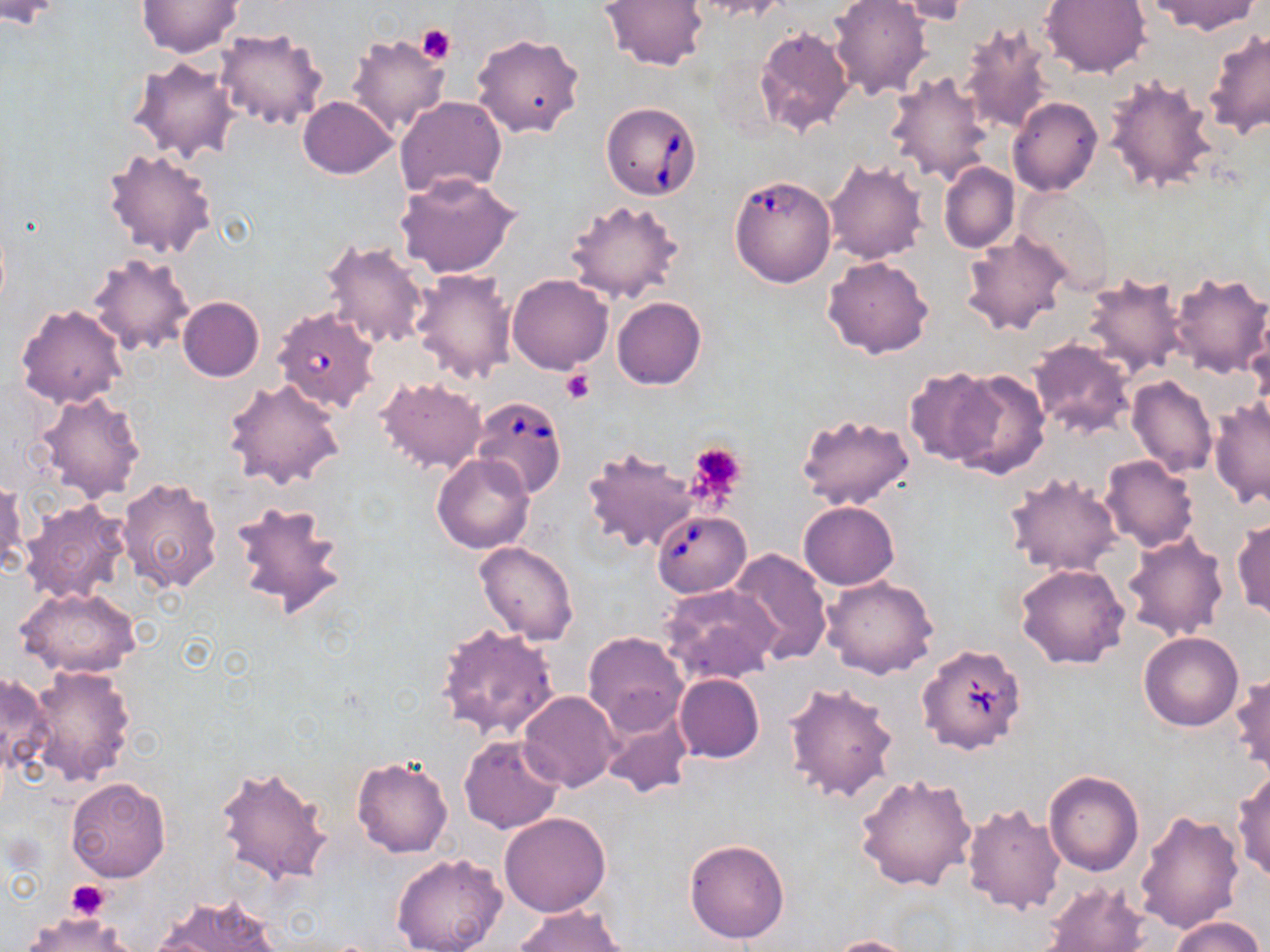
slide_level_diagnosis: Babesia divergens
preparation: thin blood smear
field_of_view: one of a larger specimen
platelet_locations: 'approximate bounding boxes as (x1,y1)-(x2,y2) corner pairs in pixels: (416,24)-(456,65), (560,370)-(594,405), (686,441)-(747,502), (66,880)-(109,920)'
magnification: 1000x
uninfected_red_blood_cell_locations: 'approximate bounding boxes as (x1,y1)-(x2,y2) corner pairs in pixels: (136,0)-(243,57), (601,0)-(709,70), (692,0)-(788,20), (828,0)-(933,102), (1041,0)-(1152,78), (1146,0)-(1260,35), (0,1)-(67,29), (887,1)-(972,26), (957,21)-(1056,136), (215,26)-(328,131), (753,26)-(855,137), (1203,30)-(1270,139), (345,33)-(450,136), (472,33)-(586,139), (127,55)-(239,162), (886,71)-(995,186), (1104,75)-(1221,195), (297,96)-(397,179), (394,96)-(507,199), (1008,98)-(1102,196), (101,146)-(219,259), (824,158)-(929,265), (939,162)-(1019,254), (395,172)-(521,278), (1015,187)-(1116,295), (565,198)-(686,305), (961,232)-(1070,338), (321,239)-(429,350), (88,252)-(196,357), (822,256)-(935,358), (410,267)-(518,385), (1081,270)-(1189,381), (1167,270)-(1270,379), (507,274)-(613,374), (177,297)-(265,382), (613,297)-(707,390), (15,303)-(128,409), (271,306)-(382,414), (1248,333)-(1270,434), (1027,339)-(1136,441), (903,366)-(1001,465), (945,368)-(1050,477), (1127,375)-(1218,478), (376,376)-(487,473), (223,377)-(347,492), (34,391)-(146,503), (1208,398)-(1269,509), (796,413)-(915,511), (582,446)-(697,555), (432,453)-(535,553), (1100,455)-(1199,552), (1005,473)-(1123,577), (116,476)-(223,592), (0,479)-(28,578), (228,496)-(349,623), (19,497)-(131,604), (798,500)-(899,591), (1232,516)-(1270,622), (1122,531)-(1228,642), (474,541)-(580,644), (728,548)-(832,663), (1015,562)-(1130,668), (821,577)-(939,679), (660,584)-(781,684), (16,587)-(143,677), (433,622)-(560,741), (583,630)-(689,733), (1139,631)-(1244,732), (25,664)-(137,788), (1231,669)-(1270,781), (0,670)-(52,779), (674,673)-(764,763), (783,680)-(899,804), (518,691)-(619,793), (598,703)-(694,800), (458,734)-(564,835), (351,757)-(453,858), (213,765)-(334,886), (1232,767)-(1270,883), (1043,770)-(1144,876), (853,772)-(978,893), (67,778)-(172,882), (960,804)-(1066,916), (1135,808)-(1245,934), (499,812)-(612,917), (684,838)-(790,944), (390,852)-(508,952), (1039,881)-(1150,952), (154,891)-(285,952), (514,905)-(630,952), (21,913)-(138,952), (1166,915)-(1266,952), (826,935)-(925,952)'
image_size: 1270×952 pixels
babesia_divergens_infected_red_blood_cell_locations: 'approximate bounding boxes as (x1,y1)-(x2,y2) corner pairs in pixels: (601,102)-(703,202), (729,174)-(837,288), (469,395)-(568,499), (651,509)-(751,598), (916,642)-(1029,755)'
modality: optical microscopy
stain: May-Grünwald-Giemsa